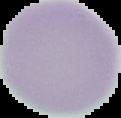

Summary:
  - Preparation: thin blood smear
  - Image size: 121×118 pixels
  - Image type: cell region segmented out of the field of view; surrounding area masked to black
  - Malaria status: uninfected